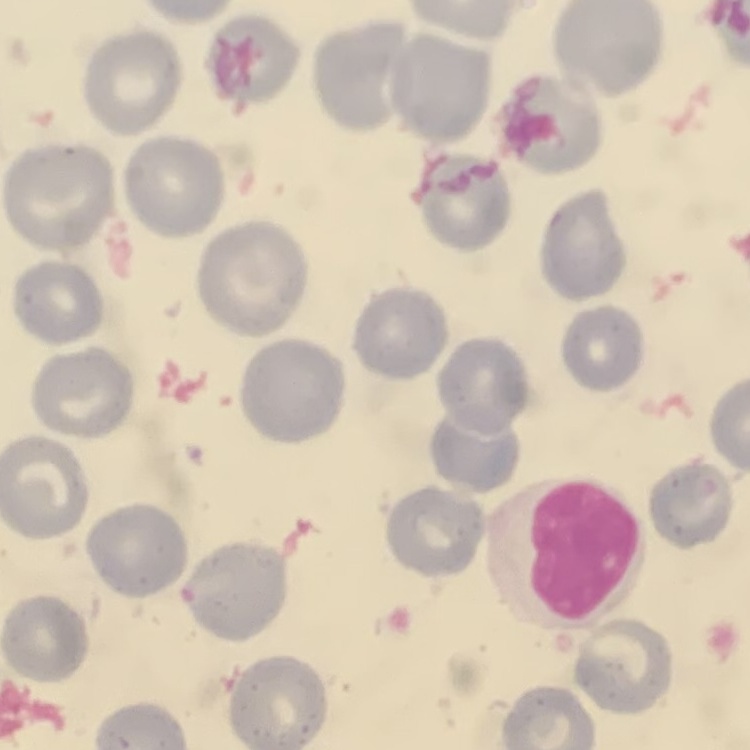

The erythrocytes exhibit no rouleaux formation. Square crop of a larger photomicrograph. Field's or Giemsa stain. Thin blood film.